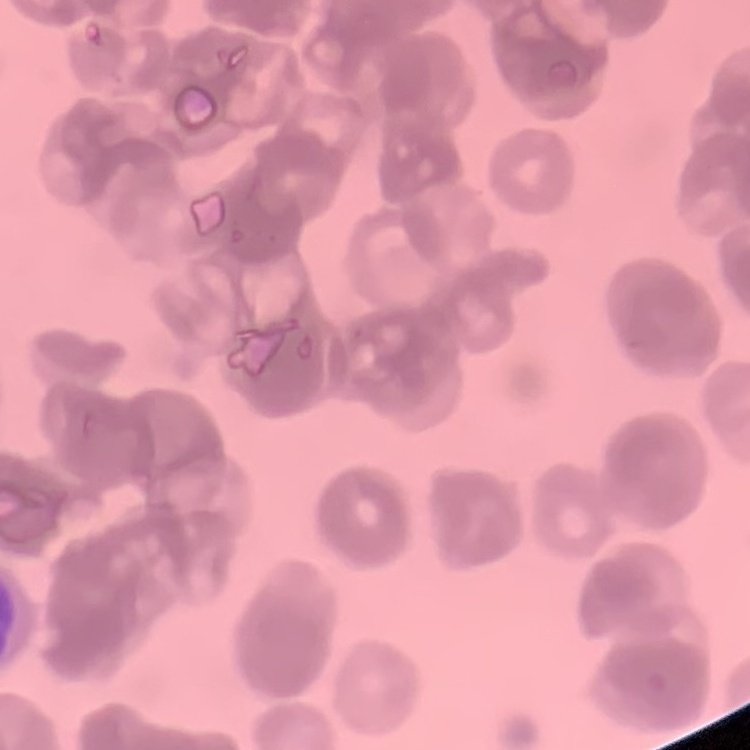

{
  "red_blood_cell_morphology": "rouleaux formation",
  "preparation": "thin peripheral smear",
  "stain": "Field's or Giemsa",
  "image_type": "square crop of a larger photomicrograph"
}